Classify this cell by malaria status.
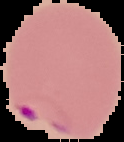
Parasitized.

Image is 124×142 pixels. Cell region segmented out of the field of view; the surrounding area is masked to black. From a thin blood smear.